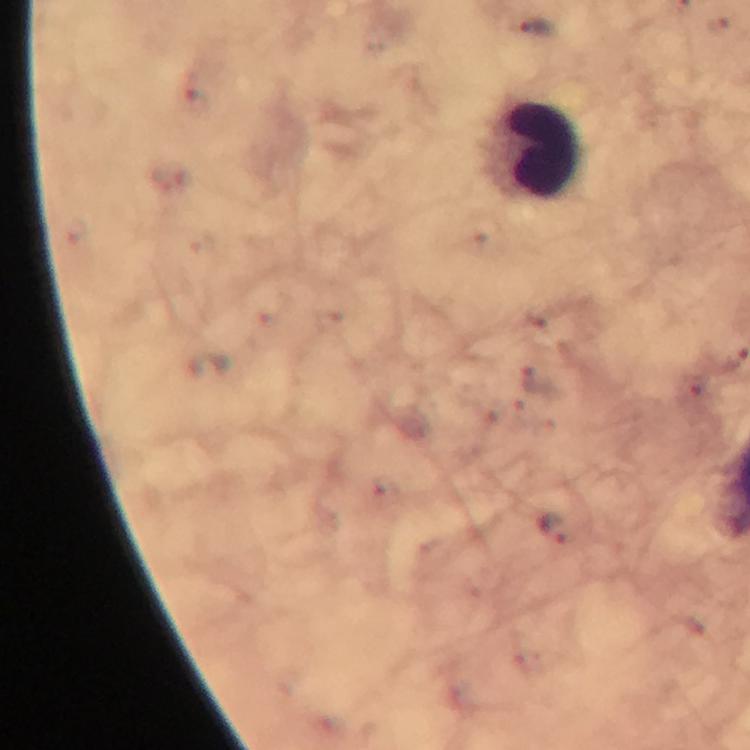
Approximate centers as (x, y) in pixels.
Summary:
  - Malaria parasite locations: (538, 28), (555, 527)
  - Leukocyte locations: (535, 150)
  - Capture: smartphone photograph through a microscope
  - Context: from a diagnostic examination for malaria
  - Preparation: thick blood smear
  - Magnification: 100x
  - Cropped from: a single field of view
  - Immersion oil: applied
  - Stain: Giemsa
  - Image size: 750×750 pixels